Identify the blood parasite species.
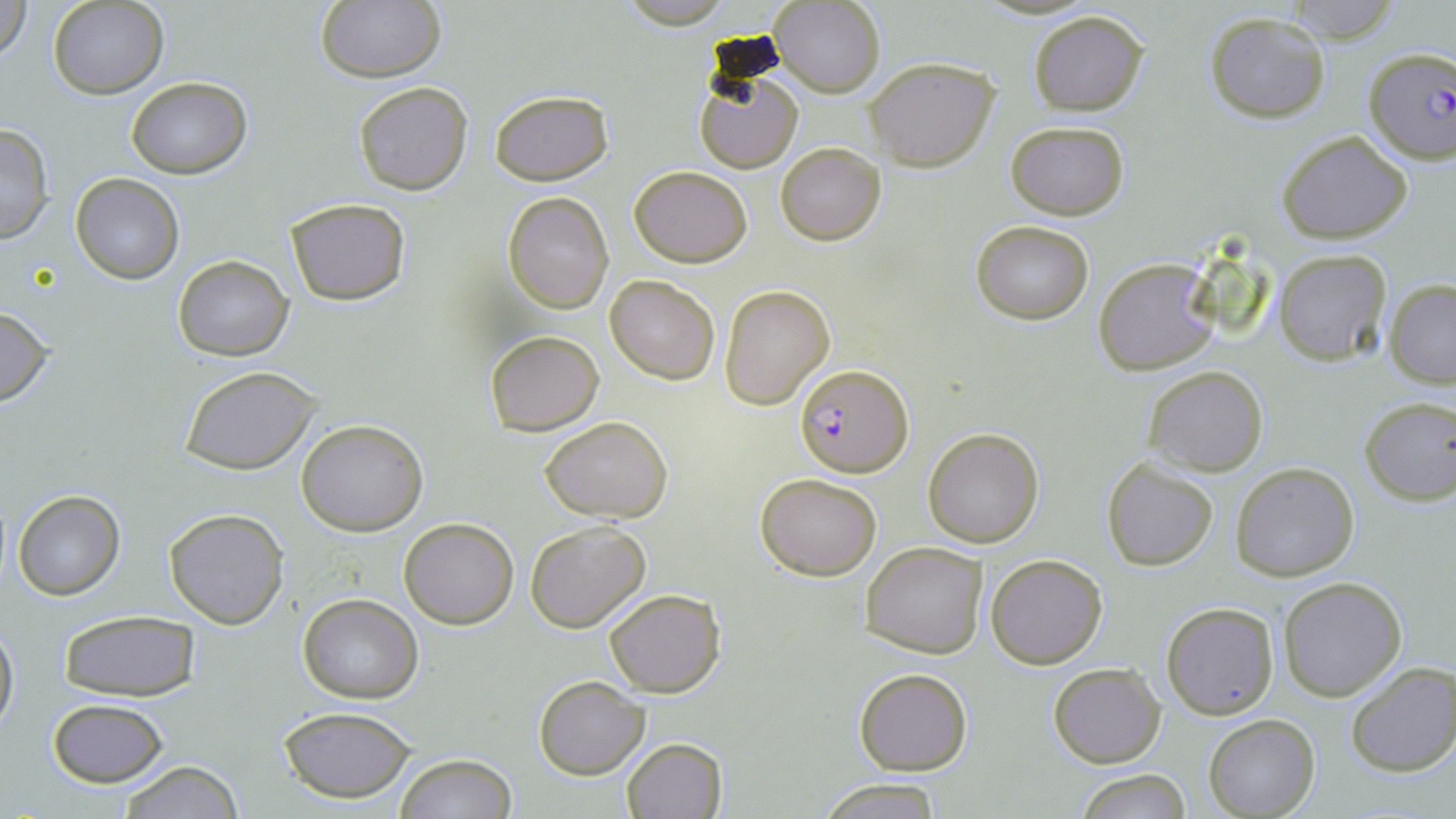
Plasmodium falciparum.

modality = optical microscopy
preparation = thin blood film
field of view = single
stain = May-Grünwald-Giemsa
image size = 1456×819 pixels
Plasmodium falciparum-infected red blood cell locations = approximate bounding boxes as [x1, y1, x2, y2] in pixels: [1362, 47, 1456, 165], [797, 363, 913, 476]
uninfected red blood cell locations = approximate bounding boxes as [x1, y1, x2, y2] in pixels: [0, 0, 33, 60], [48, 0, 167, 98], [1282, 0, 1403, 42], [770, 1, 885, 97], [314, 2, 446, 83], [1027, 9, 1149, 116], [1202, 11, 1332, 122], [865, 57, 999, 170], [693, 66, 803, 173], [125, 75, 253, 180], [352, 81, 473, 195], [487, 90, 614, 186], [1004, 121, 1130, 219], [0, 122, 54, 243], [1275, 129, 1412, 244], [775, 143, 886, 245], [629, 165, 752, 266], [70, 173, 183, 282], [503, 190, 613, 313], [285, 198, 412, 306], [970, 218, 1093, 326], [1273, 249, 1392, 365], [172, 253, 294, 362], [1092, 256, 1219, 377], [605, 275, 719, 384], [1384, 279, 1456, 388], [719, 284, 834, 409], [0, 304, 55, 408], [484, 330, 605, 437], [179, 364, 325, 476], [1142, 365, 1269, 477], [1358, 395, 1456, 505], [539, 416, 673, 522], [297, 420, 427, 536], [922, 426, 1045, 548], [1101, 456, 1218, 570], [1231, 461, 1359, 581], [757, 472, 882, 580], [12, 490, 124, 600], [164, 508, 289, 628], [399, 517, 519, 629], [524, 521, 651, 634], [862, 541, 988, 659], [986, 552, 1108, 669], [1277, 576, 1408, 701], [602, 588, 726, 697], [297, 594, 423, 703], [1161, 603, 1280, 719], [58, 610, 201, 702], [1, 618, 18, 740], [1047, 661, 1165, 768], [1345, 662, 1456, 778], [854, 667, 972, 776], [534, 677, 649, 779], [47, 697, 173, 788], [278, 706, 417, 804], [1204, 714, 1319, 818], [621, 737, 726, 818], [395, 753, 517, 819], [116, 761, 245, 818], [1074, 767, 1194, 819], [819, 778, 939, 817]
magnification = 1000x